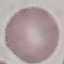

Summary:
  - Result: negative for malaria parasites
  - Preparation: thin smear
  - Stain: Giemsa
  - Image type: automatically extracted cell patch, resized to 64 × 64 pixels
  - Capture: smartphone through the microscope eyepiece